Locate every blood parasite and identify its species.
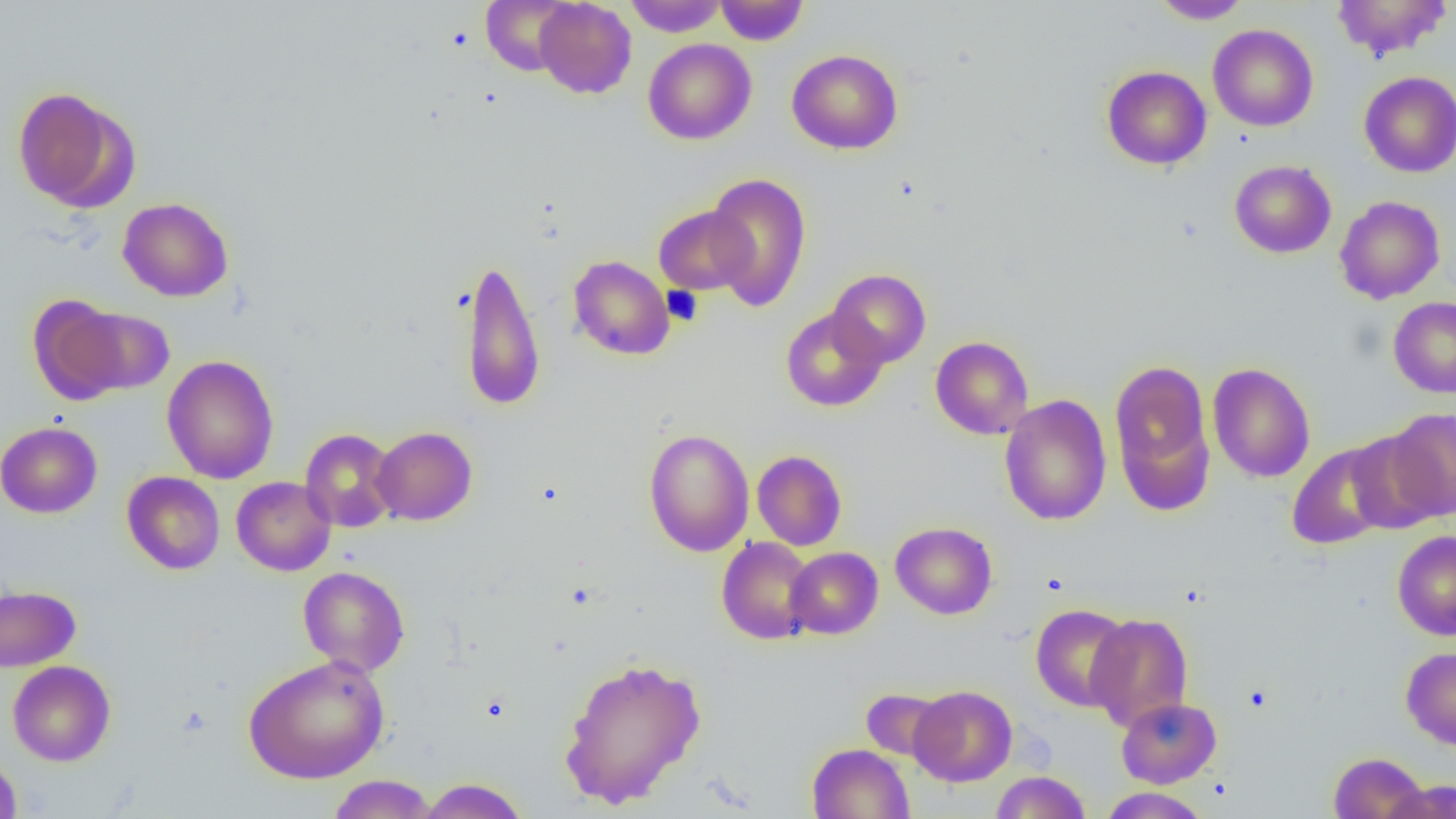
No blood parasites seen.

Summary:
  - Coordinate format: approximate bounding boxes as named x1/y1/x2/y2 corners in pixels
  - Platelet locations: (x1=662, y1=286, x2=703, y2=326)
  - Uninfected red blood cell locations: (x1=481, y1=0, x2=577, y2=76), (x1=624, y1=0, x2=727, y2=36), (x1=715, y1=0, x2=808, y2=45), (x1=1150, y1=0, x2=1251, y2=24), (x1=1331, y1=0, x2=1451, y2=60), (x1=534, y1=1, x2=636, y2=98), (x1=1208, y1=24, x2=1319, y2=131), (x1=643, y1=38, x2=757, y2=144), (x1=787, y1=49, x2=903, y2=155), (x1=1101, y1=65, x2=1211, y2=170), (x1=1358, y1=71, x2=1456, y2=177), (x1=13, y1=87, x2=134, y2=211), (x1=1229, y1=160, x2=1336, y2=258), (x1=704, y1=172, x2=812, y2=311), (x1=1334, y1=196, x2=1446, y2=304), (x1=117, y1=197, x2=233, y2=302), (x1=654, y1=205, x2=756, y2=294), (x1=460, y1=255, x2=546, y2=412), (x1=568, y1=255, x2=675, y2=360), (x1=827, y1=269, x2=931, y2=368), (x1=28, y1=295, x2=130, y2=405), (x1=1388, y1=296, x2=1456, y2=397), (x1=73, y1=306, x2=174, y2=395), (x1=780, y1=307, x2=888, y2=412), (x1=931, y1=336, x2=1033, y2=440), (x1=161, y1=355, x2=279, y2=484), (x1=1109, y1=357, x2=1214, y2=501), (x1=1207, y1=362, x2=1315, y2=482), (x1=999, y1=395, x2=1112, y2=525), (x1=1385, y1=409, x2=1456, y2=520), (x1=0, y1=421, x2=102, y2=518), (x1=371, y1=426, x2=477, y2=525), (x1=300, y1=428, x2=400, y2=533), (x1=644, y1=428, x2=755, y2=557), (x1=1345, y1=430, x2=1443, y2=534), (x1=1287, y1=442, x2=1395, y2=550), (x1=752, y1=450, x2=847, y2=550), (x1=121, y1=472, x2=225, y2=575), (x1=231, y1=476, x2=336, y2=576), (x1=891, y1=522, x2=997, y2=619), (x1=1392, y1=530, x2=1456, y2=640), (x1=716, y1=537, x2=817, y2=644), (x1=785, y1=547, x2=883, y2=639), (x1=298, y1=566, x2=410, y2=676), (x1=0, y1=585, x2=81, y2=671), (x1=1030, y1=603, x2=1134, y2=711), (x1=1085, y1=613, x2=1194, y2=731), (x1=1400, y1=647, x2=1456, y2=749), (x1=243, y1=654, x2=390, y2=784), (x1=558, y1=656, x2=707, y2=809), (x1=7, y1=660, x2=116, y2=765), (x1=909, y1=685, x2=1017, y2=787), (x1=860, y1=689, x2=950, y2=763), (x1=1116, y1=697, x2=1221, y2=788), (x1=806, y1=743, x2=914, y2=819), (x1=1328, y1=752, x2=1429, y2=819), (x1=0, y1=753, x2=22, y2=818), (x1=991, y1=771, x2=1091, y2=818), (x1=327, y1=774, x2=439, y2=818), (x1=417, y1=778, x2=530, y2=818), (x1=1384, y1=778, x2=1456, y2=819), (x1=1099, y1=787, x2=1210, y2=818)
  - Slide-level diagnosis: negative for blood parasites
  - Magnification: 1000x
  - Modality: optical microscopy
  - Field of view: one of a larger specimen
  - Image size: 1456×819 pixels
  - Preparation: thin blood film